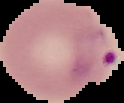
Summary:
  - Preparation: thin blood smear
  - Image type: cell region segmented out of the field of view; surrounding area masked to black
  - Image size: 124×103 pixels
  - Malaria status: parasitized